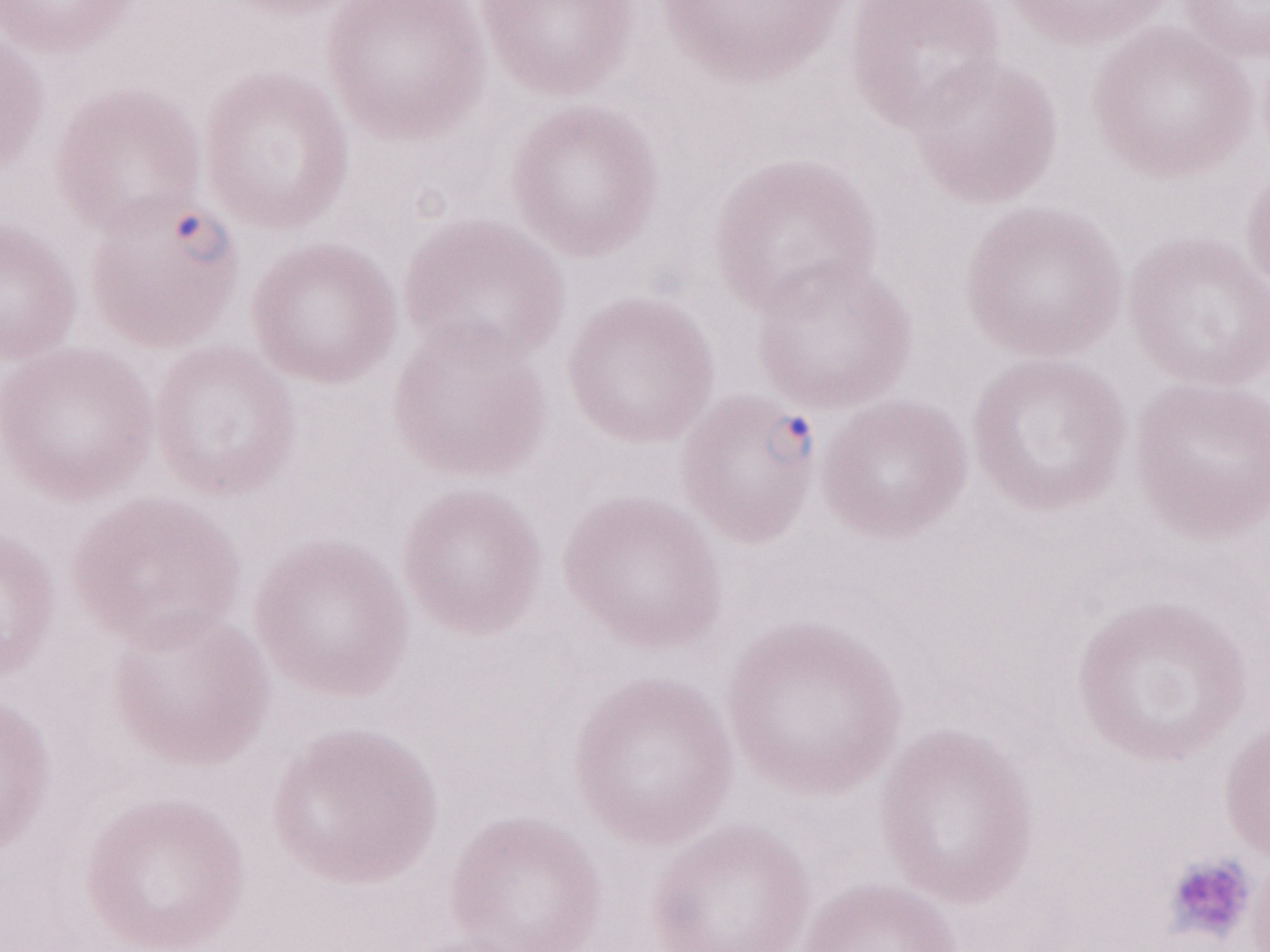
Image is 1270×952 pixels. One field of this slide. May-Grünwald-Giemsa (MGG) stain. 1,000x magnification. Malaria diagnosis (patient-level): positive. Olympus BX43 microscope, Olympus DP73 camera. Thin peripheral-blood smear.